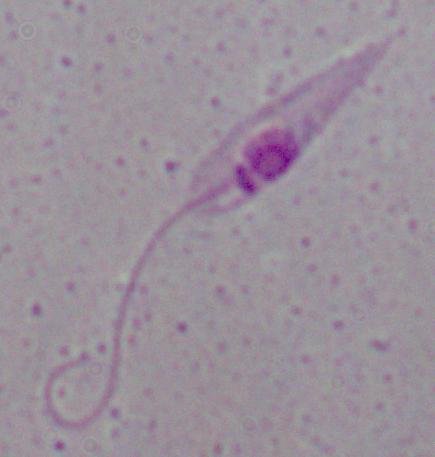
Captured at 1000x magnification. A Leishmania parasite is shown. Photomicrograph.